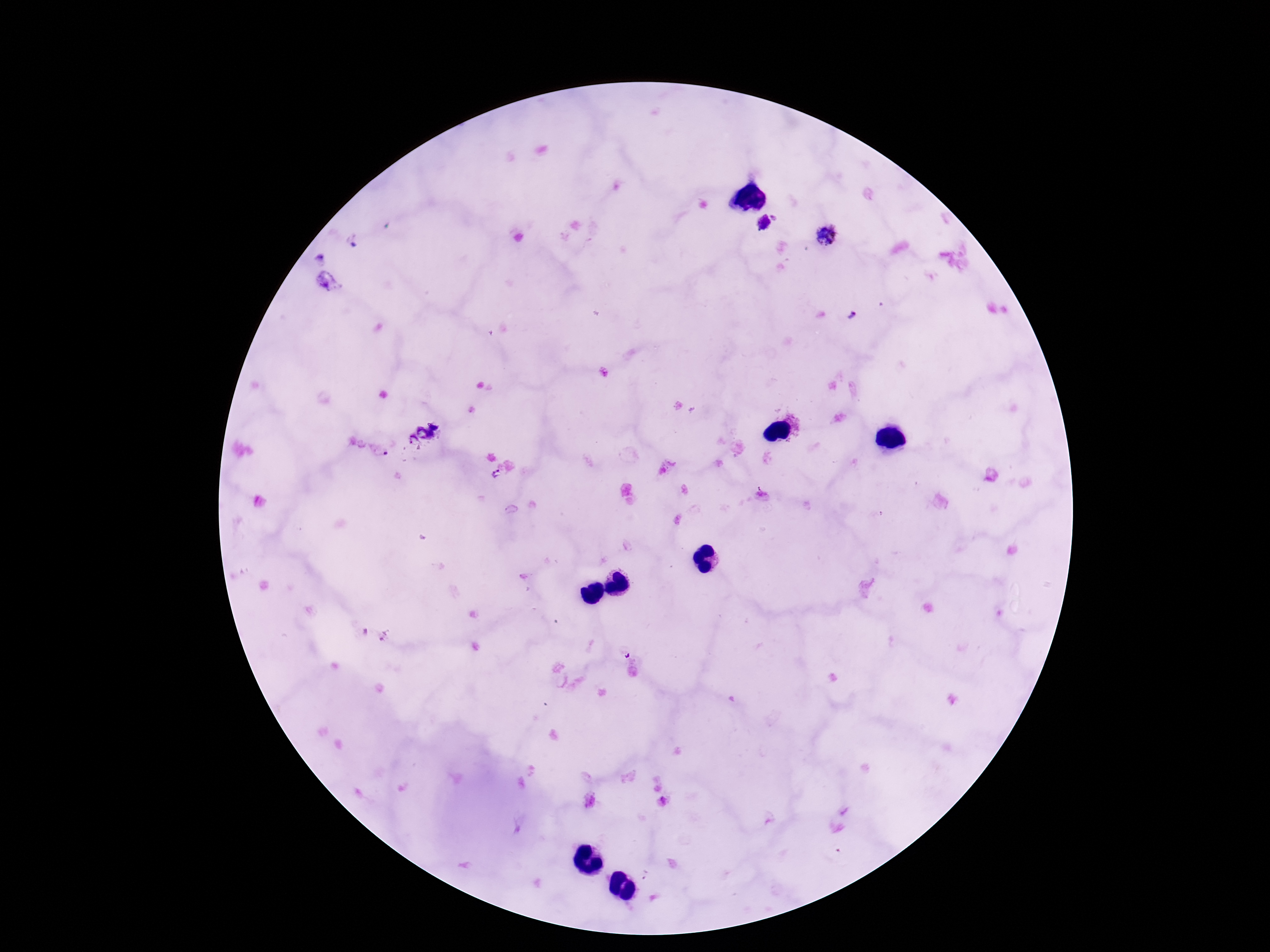
Approximate object centers, in pixels from the top-left corner. Plasmodium parasite locations: (x=764, y=224), (x=825, y=236), (x=436, y=424), (x=423, y=433), (x=412, y=440), (x=495, y=475). Giemsa stain. Smartphone photograph taken through the microscope eyepiece. Image is 1270×952 pixels. 100x magnification. Patient malaria status: infected. One field from this slide. Thick blood smear.